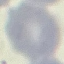
{
  "result": "negative for malaria parasites",
  "preparation": "thin smear",
  "capture": "smartphone camera at the microscope eyepiece",
  "stain": "Giemsa",
  "image_type": "automatically extracted cell patch, resized to 64 × 64 pixels"
}